Locate and identify every blood parasite.
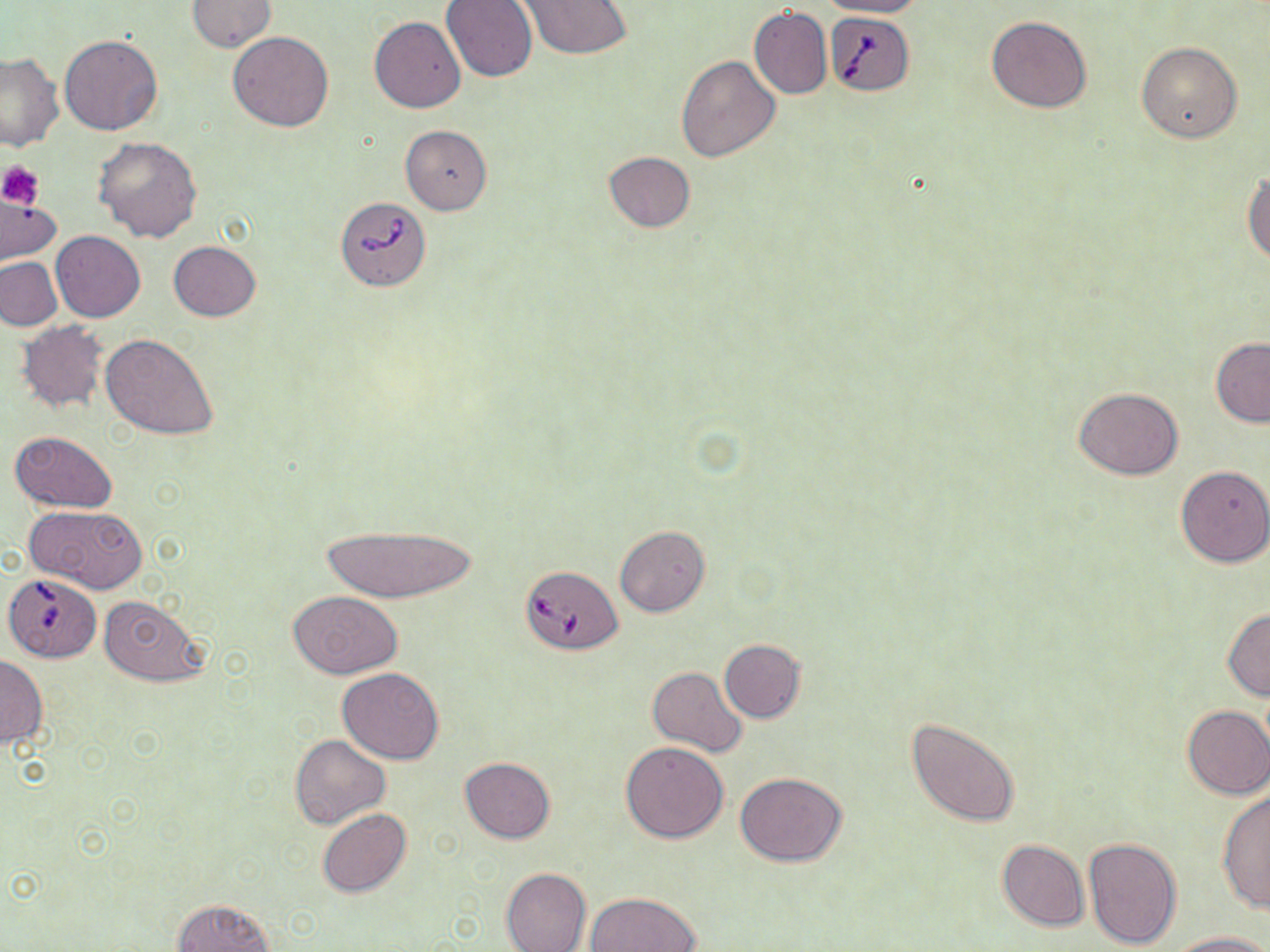
Approximate bounding boxes as [x1, y1, x2, y2] in pixels.
Babesia divergens-infected red blood cells: [826, 11, 914, 96], [336, 196, 431, 291], [520, 564, 624, 655], [4, 572, 101, 663].
No Plasmodium falciparum, Plasmodium ovale, Plasmodium malariae, Plasmodium vivax, or Trypanosoma brucei observed.

Platelet locations: [1, 162, 46, 209]. Uninfected red blood cell locations: [818, 0, 929, 19], [186, 1, 276, 51], [440, 1, 538, 82], [517, 1, 632, 59], [750, 6, 832, 99], [987, 15, 1091, 113], [370, 16, 466, 114], [228, 32, 334, 132], [59, 35, 164, 136], [1136, 42, 1242, 142], [1, 51, 65, 151], [674, 53, 780, 162], [401, 125, 493, 215], [93, 137, 203, 242], [603, 151, 696, 232], [1244, 171, 1270, 266], [1, 199, 62, 262], [51, 231, 146, 321], [168, 241, 261, 321], [0, 257, 63, 332], [16, 321, 108, 414], [102, 333, 220, 440], [1210, 338, 1270, 427], [1074, 387, 1183, 480], [9, 431, 118, 512], [1175, 464, 1269, 568], [25, 504, 148, 594], [314, 522, 481, 604], [615, 525, 710, 617], [288, 590, 401, 678], [97, 594, 209, 687], [1223, 608, 1270, 700], [718, 638, 805, 722], [0, 655, 46, 750], [647, 666, 747, 757], [337, 667, 444, 764], [1181, 705, 1270, 799], [906, 716, 1020, 827], [291, 735, 391, 828], [620, 741, 729, 843], [459, 757, 555, 844], [735, 772, 846, 867], [1217, 790, 1269, 911], [316, 809, 411, 897], [1083, 837, 1182, 949], [997, 839, 1088, 931], [500, 866, 592, 952], [585, 892, 701, 952], [172, 898, 276, 951], [1167, 931, 1268, 952]. Slide-level diagnosis: Babesia divergens. 1000x magnification. Image is 1270×952 pixels. Thin blood film. One field of a larger specimen. Optical microscopy. May-Grünwald-Giemsa-stained preparation.